Assess this cell for malaria.
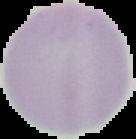

It is uninfected.

image_type: segmented cell region on a black background
preparation: thin blood smear
image_size: 136×139 pixels